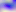

magnification = 400x
modality = micrograph
identification = Toxoplasma gondii